Assess this cell for malaria.
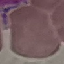
It is uninfected.

{
  "preparation": "thin blood smear",
  "image_type": "automatically extracted cell patch, resized to 64 × 64 pixels",
  "stain": "Giemsa",
  "capture": "smartphone camera at the microscope eyepiece"
}